Locate and identify every blood parasite.
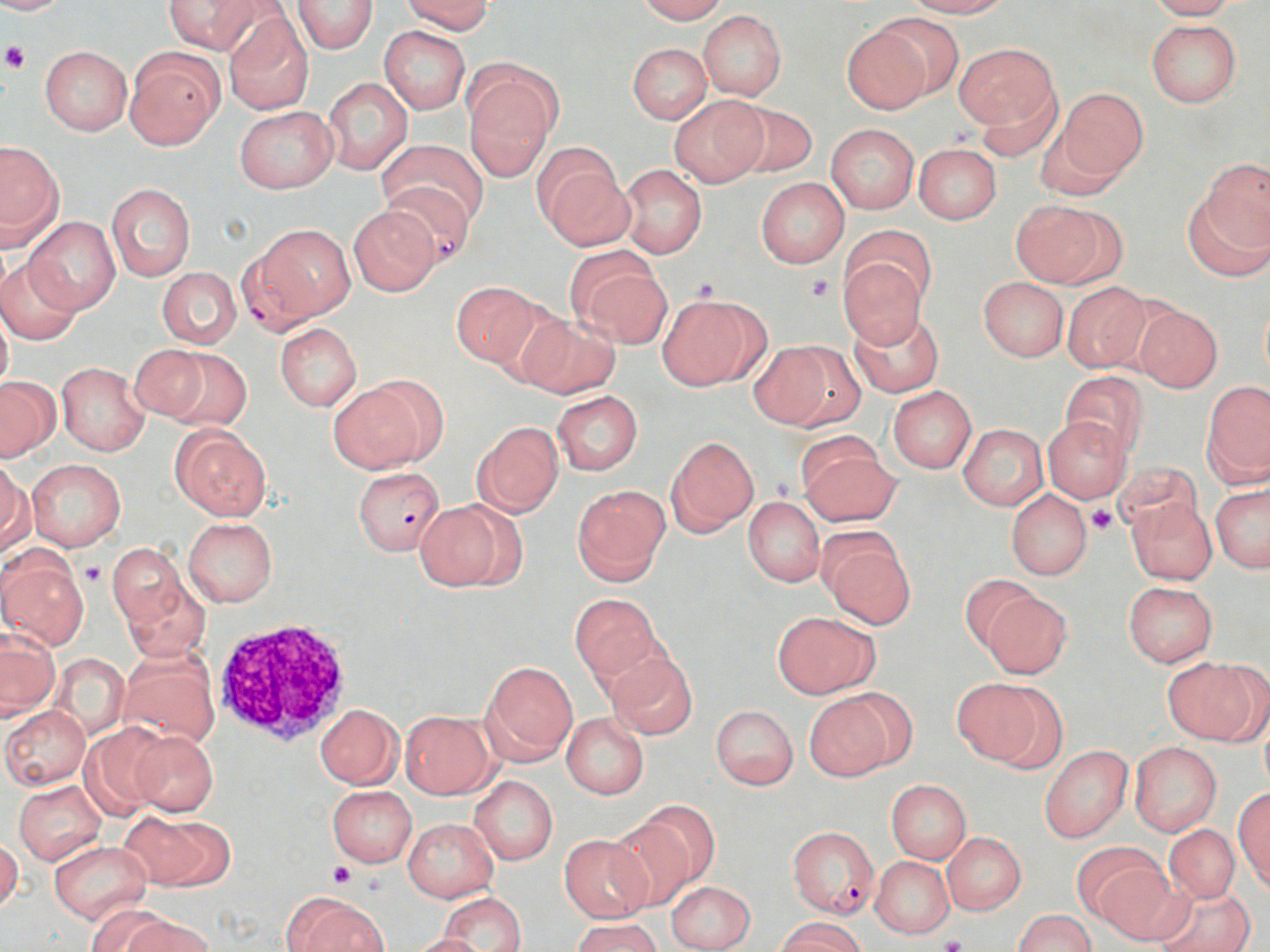

Approximate bounding boxes as [x1, y1, x2, y2] in pixels.
Plasmodium falciparum-infected red blood cells: [382, 182, 477, 268], [239, 225, 354, 335], [353, 466, 446, 556], [786, 826, 879, 918].
No Plasmodium ovale, Plasmodium malariae, Plasmodium vivax, Babesia divergens, or Trypanosoma brucei observed.

Summary:
  - Platelet locations: [3, 42, 30, 73], [804, 274, 837, 303], [689, 276, 721, 303], [1087, 504, 1116, 533], [81, 563, 105, 586], [329, 862, 355, 888], [939, 935, 967, 952]
  - White blood cell locations: [210, 618, 354, 747]
  - Uninfected red blood cell locations: [0, 0, 76, 15], [165, 0, 264, 55], [401, 0, 494, 34], [636, 0, 727, 23], [905, 0, 1012, 17], [1147, 0, 1238, 20], [171, 1, 305, 89], [293, 1, 379, 54], [223, 9, 313, 114], [697, 9, 787, 100], [871, 12, 965, 101], [1145, 19, 1242, 107], [841, 22, 933, 114], [377, 26, 471, 114], [627, 43, 711, 124], [953, 43, 1059, 134], [40, 45, 132, 135], [125, 47, 223, 150], [323, 76, 413, 174], [465, 79, 553, 180], [1055, 88, 1147, 185], [669, 95, 768, 187], [731, 101, 818, 179], [234, 106, 336, 193], [825, 123, 919, 215], [378, 138, 490, 229], [0, 141, 63, 249], [913, 143, 1001, 223], [534, 146, 629, 247], [1198, 157, 1270, 258], [618, 165, 708, 259], [755, 177, 849, 268], [107, 183, 196, 281], [1184, 194, 1269, 282], [1011, 198, 1118, 288], [348, 205, 440, 296], [23, 217, 120, 316], [842, 223, 936, 309], [570, 250, 672, 347], [0, 251, 84, 345], [837, 255, 930, 348], [155, 267, 241, 349], [977, 277, 1069, 361], [449, 280, 546, 368], [1061, 280, 1154, 373], [657, 295, 768, 391], [1259, 295, 1270, 384], [1131, 303, 1223, 392], [0, 304, 13, 398], [849, 308, 945, 398], [513, 312, 621, 399], [275, 323, 361, 411], [748, 342, 852, 431], [148, 344, 252, 431], [55, 361, 151, 456], [1060, 371, 1149, 460], [0, 376, 60, 461], [1202, 380, 1270, 486], [328, 381, 433, 473], [888, 387, 976, 473], [551, 391, 644, 475], [1041, 415, 1133, 503], [471, 421, 564, 518], [957, 423, 1047, 511], [170, 425, 271, 522], [796, 434, 898, 527], [666, 436, 758, 536], [0, 458, 32, 555], [26, 458, 126, 550], [1110, 460, 1203, 538], [1210, 483, 1269, 573], [572, 484, 669, 585], [1006, 489, 1093, 581], [742, 497, 824, 586], [1128, 498, 1216, 584], [414, 499, 519, 591], [182, 516, 278, 606], [818, 530, 915, 627], [104, 542, 186, 630], [0, 549, 89, 650], [960, 574, 1039, 651], [123, 578, 210, 663], [1123, 582, 1216, 666], [982, 591, 1072, 679], [569, 593, 661, 685], [583, 599, 684, 734], [772, 612, 879, 699], [1, 632, 59, 720], [606, 649, 698, 740], [120, 651, 219, 746], [50, 652, 129, 741], [1167, 658, 1265, 747], [480, 660, 577, 763], [952, 678, 1062, 770], [802, 692, 898, 781], [314, 704, 402, 789], [711, 705, 797, 789], [2, 706, 89, 789], [400, 711, 495, 798], [561, 713, 649, 799], [80, 723, 170, 818], [131, 731, 218, 817], [1130, 741, 1221, 835], [1040, 746, 1132, 842], [468, 775, 558, 865], [884, 779, 972, 863], [13, 780, 106, 866], [326, 785, 417, 866], [1234, 787, 1269, 891], [122, 811, 230, 892], [603, 812, 702, 912], [401, 817, 500, 902], [1164, 824, 1241, 903], [942, 833, 1026, 915], [559, 835, 651, 922], [0, 837, 23, 916], [49, 840, 152, 923], [1072, 840, 1166, 929], [870, 855, 954, 939], [1095, 865, 1189, 946], [666, 880, 755, 951], [1152, 885, 1255, 952], [281, 892, 388, 951], [437, 892, 527, 952], [85, 904, 178, 952], [1013, 910, 1094, 952], [124, 914, 212, 952], [571, 917, 662, 952], [778, 917, 867, 952], [409, 932, 488, 952]
  - Slide-level diagnosis: Plasmodium falciparum
  - Image size: 1270×952 pixels
  - Preparation: thin blood smear
  - Field of view: single
  - Stain: May-Grünwald-Giemsa
  - Modality: optical microscopy
  - Magnification: 1000x